Name the blood parasite species.
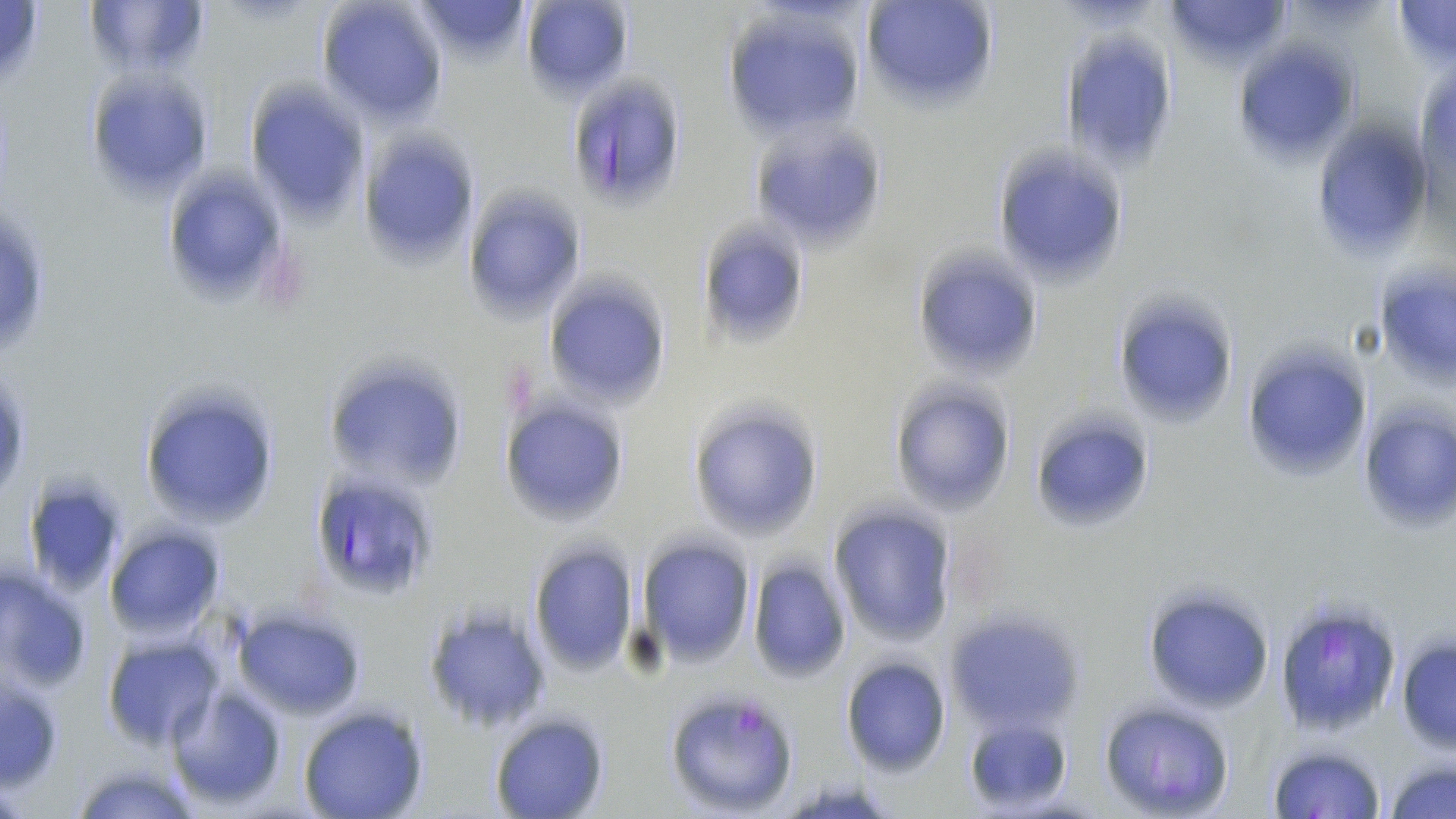
Plasmodium falciparum.

Approximate bounding boxes as (x1,y1)-(x2,y2) corner pairs in pixels. Plasmodium falciparum-infected red blood cell locations: (564,73)-(690,209), (307,468)-(441,601), (1273,597)-(1404,739), (664,688)-(803,816). Uninfected red blood cell locations: (83,0)-(210,81), (316,0)-(448,126), (414,0)-(533,64), (519,0)-(635,104), (859,0)-(1001,115), (1162,0)-(1290,69), (1392,0)-(1456,70), (0,1)-(47,86), (723,5)-(869,139), (1059,33)-(1181,171), (1235,42)-(1359,165), (84,69)-(216,199), (245,82)-(370,222), (750,121)-(888,254), (1313,122)-(1436,259), (362,129)-(479,268), (992,142)-(1132,289), (158,166)-(293,306), (463,187)-(585,321), (697,217)-(811,347), (911,245)-(1046,381), (545,278)-(670,409), (1381,282)-(1456,381), (1108,291)-(1241,431), (1242,342)-(1374,483), (321,356)-(469,490), (138,381)-(279,535), (889,382)-(1015,516), (500,397)-(631,526), (688,401)-(824,544), (1025,407)-(1159,538), (1365,411)-(1456,533), (29,487)-(123,594), (829,505)-(957,645), (105,527)-(226,641), (636,534)-(756,667), (527,538)-(640,677), (746,558)-(851,682), (0,565)-(92,692), (1143,585)-(1277,712), (420,598)-(553,731), (230,605)-(368,720), (944,611)-(1084,734), (1395,636)-(1456,752), (102,637)-(222,751), (840,656)-(951,776), (0,676)-(63,788), (167,684)-(288,809), (1099,701)-(1235,817), (297,706)-(428,819), (489,712)-(609,819), (1265,743)-(1385,819), (1384,759)-(1456,819), (70,762)-(197,817). Image is 1456×819 pixels. May-Grünwald-Giemsa stain. 1000x magnification. One field of a larger specimen. Thin blood film. Light microscopy.